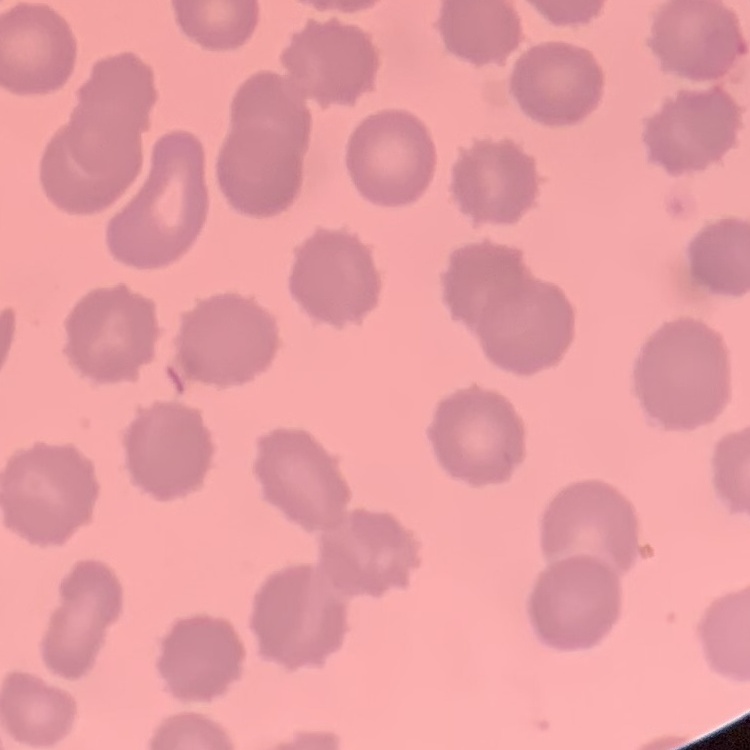 The erythrocytes show no rouleaux formation. Thin blood smear. One tile cut from a larger photomicrograph. Stained with either Field's or Giemsa.